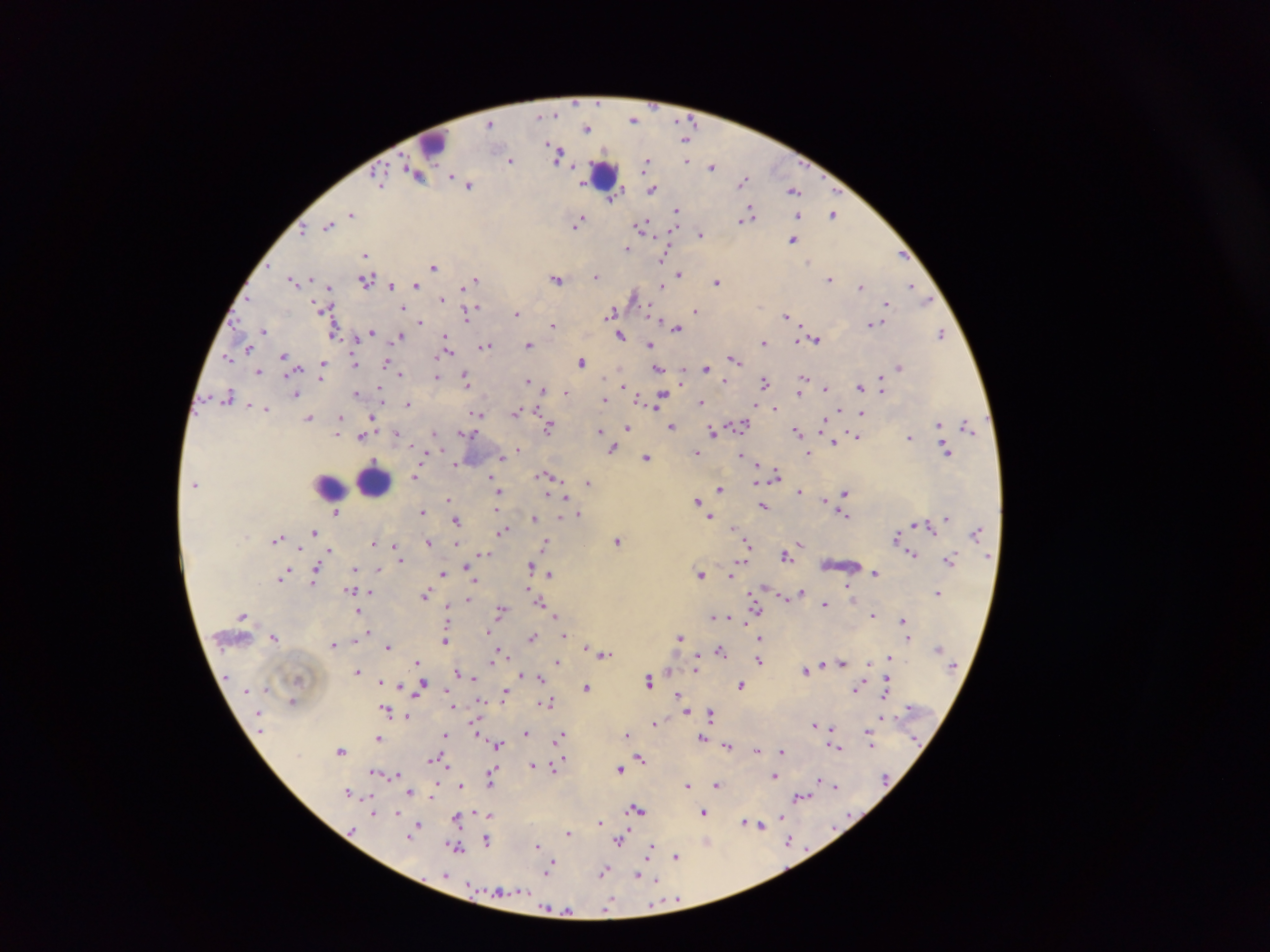

plasmodium_parasite_locations: 'approximate centers as {x, y} in pixels: {635, 120}, {490, 123}, {588, 128}, {686, 137}, {557, 154}, {512, 160}, {687, 160}, {646, 163}, {573, 166}, {713, 167}, {416, 173}, {379, 178}, {745, 180}, {469, 185}, {653, 188}, {794, 190}, {617, 191}, {613, 198}, {677, 210}, {351, 214}, {834, 214}, {798, 215}, {748, 217}, {579, 221}, {329, 225}, {643, 227}, {303, 228}, {701, 233}, {793, 238}, {627, 249}, {902, 254}, {365, 255}, {664, 256}, {434, 265}, {680, 273}, {597, 276}, {557, 278}, {830, 279}, {294, 280}, {366, 280}, {475, 280}, {717, 281}, {470, 283}, {392, 285}, {416, 285}, {662, 285}, {861, 286}, {911, 286}, {329, 288}, {635, 295}, {921, 295}, {442, 299}, {927, 301}, {887, 305}, {403, 307}, {474, 308}, {326, 309}, {697, 311}, {517, 313}, {467, 314}, {612, 314}, {786, 315}, {420, 321}, {872, 322}, {553, 326}, {677, 328}, {334, 330}, {263, 331}, {371, 331}, {941, 333}, {620, 335}, {401, 336}, {357, 338}, {447, 338}, {815, 339}, {764, 341}, {529, 344}, {650, 344}, {249, 346}, {485, 346}, {446, 353}, {285, 356}, {228, 357}, {734, 358}, {583, 361}, {355, 362}, {386, 362}, {323, 364}, {706, 366}, {900, 366}, {659, 368}, {259, 370}, {400, 374}, {322, 376}, {438, 377}, {803, 377}, {882, 378}, {467, 379}, {726, 380}, {528, 381}, {681, 382}, {766, 382}, {623, 385}, {860, 386}, {826, 388}, {542, 390}, {882, 390}, {567, 392}, {801, 392}, {356, 393}, {381, 393}, {296, 394}, {229, 396}, {639, 398}, {661, 398}, {381, 399}, {605, 399}, {702, 401}, {409, 404}, {759, 406}, {266, 408}, {775, 408}, {840, 410}, {517, 412}, {862, 412}, {478, 414}, {340, 417}, {372, 417}, {310, 418}, {741, 424}, {940, 424}, {672, 425}, {824, 425}, {968, 425}, {548, 427}, {627, 427}, {339, 428}, {599, 430}, {713, 431}, {798, 431}, {396, 432}, {434, 432}, {339, 433}, {466, 434}, {857, 435}, {362, 436}, {910, 437}, {834, 441}, {613, 448}, {519, 449}, {947, 451}, {697, 452}, {808, 453}, {503, 455}, {742, 455}, {647, 456}, {457, 463}, {548, 474}, {776, 474}, {416, 476}, {758, 481}, {588, 482}, {493, 484}, {719, 487}, {799, 491}, {498, 492}, {845, 493}, {550, 495}, {564, 496}, {449, 498}, {826, 500}, {698, 501}, {763, 507}, {337, 511}, {422, 511}, {497, 511}, {578, 514}, {843, 515}, {711, 516}, {560, 517}, {948, 518}, {534, 519}, {457, 520}, {917, 524}, {734, 529}, {503, 530}, {315, 532}, {976, 532}, {897, 536}, {278, 539}, {617, 541}, {428, 542}, {374, 543}, {457, 543}, {546, 543}, {800, 543}, {394, 545}, {748, 545}, {795, 547}, {301, 549}, {330, 550}, {398, 551}, {484, 553}, {913, 553}, {328, 555}, {786, 555}, {744, 557}, {401, 559}, {950, 560}, {531, 566}, {467, 567}, {354, 568}, {377, 569}, {316, 571}, {701, 573}, {875, 573}, {443, 574}, {551, 574}, {732, 574}, {285, 575}, {282, 578}, {474, 580}, {315, 581}, {848, 584}, {351, 589}, {528, 590}, {369, 591}, {802, 591}, {756, 592}, {938, 592}, {427, 594}, {752, 596}, {784, 597}, {468, 599}, {755, 602}, {541, 603}, {826, 604}, {756, 606}, {448, 609}, {501, 609}, {359, 611}, {873, 614}, {714, 615}, {555, 616}, {723, 616}, {730, 617}, {745, 620}, {902, 620}, {369, 631}, {490, 631}, {564, 635}, {532, 636}, {275, 637}, {761, 637}, {680, 638}, {908, 638}, {446, 639}, {354, 640}, {334, 644}, {387, 646}, {585, 647}, {721, 650}, {501, 653}, {604, 654}, {889, 657}, {496, 658}, {870, 660}, {557, 661}, {760, 661}, {418, 662}, {842, 662}, {823, 664}, {696, 669}, {357, 670}, {667, 670}, {805, 671}, {456, 672}, {522, 675}, {472, 676}, {540, 678}, {299, 679}, {380, 680}, {649, 680}, {887, 680}, {396, 682}, {742, 685}, {401, 686}, {587, 687}, {857, 688}, {267, 690}, {886, 690}, {420, 693}, {505, 694}, {678, 694}, {293, 700}, {543, 702}, {550, 702}, {453, 705}, {687, 710}, {387, 711}, {711, 713}, {407, 716}, {882, 717}, {655, 723}, {815, 724}, {831, 727}, {477, 732}, {526, 732}, {447, 734}, {628, 734}, {561, 735}, {702, 737}, {379, 738}, {870, 740}, {497, 744}, {728, 745}, {837, 747}, {342, 749}, {757, 749}, {782, 750}, {434, 758}, {641, 758}, {561, 760}, {443, 763}, {557, 763}, {533, 765}, {447, 766}, {620, 769}, {492, 772}, {554, 772}, {378, 773}, {396, 774}, {775, 776}, {490, 778}, {820, 781}, {689, 784}, {717, 784}, {460, 786}, {836, 786}, {410, 791}, {348, 792}, {433, 795}, {801, 796}, {637, 808}, {704, 811}, {374, 813}, {489, 814}, {781, 816}, {457, 817}, {599, 822}, {746, 822}, {418, 824}, {758, 824}, {568, 833}, {409, 836}, {487, 840}, {621, 840}, {790, 841}, {707, 842}, {537, 845}, {457, 847}, {651, 849}, {677, 856}, {550, 864}, {604, 871}, {446, 874}, {639, 875}, {652, 878}, {678, 899}, {610, 906}, {555, 910}, {564, 910}'
leukocyte_locations: 'approximate centers as {x, y} in pixels: {432, 142}, {604, 175}, {373, 482}, {331, 485}'
image_size: 1270×952 pixels
preparation: thick blood film
field_of_view: single
capture: mobile-phone photograph through a microscope
country: Ghana